Give the extent of all Babesia divergens-infected red blood cells.
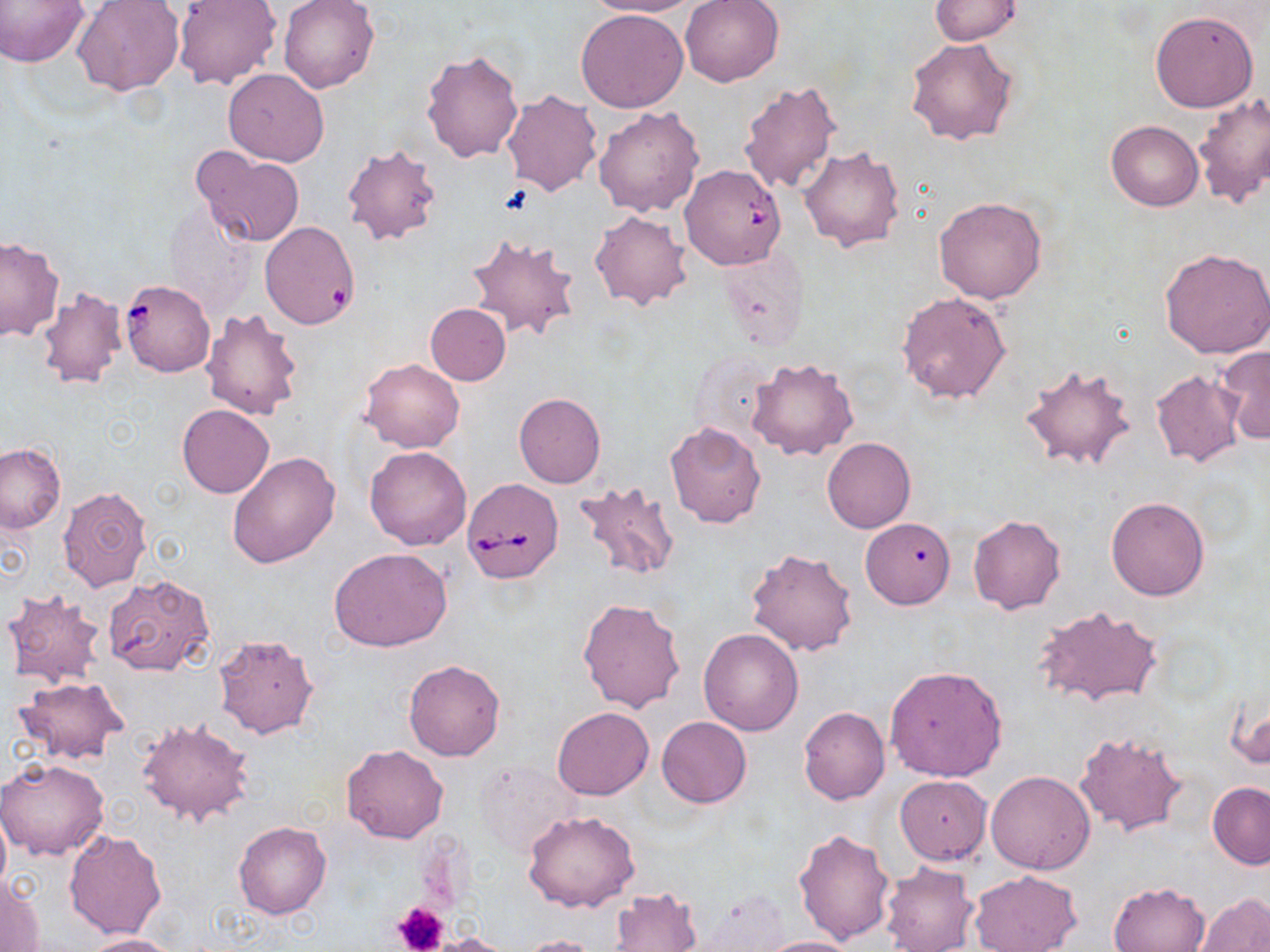

Approximate bounding boxes as (x1, y1, x2, y2) in pixels.
Babesia divergens-infected red blood cells: (678, 164, 786, 269), (119, 278, 216, 377), (461, 479, 565, 585).

Summary:
  - Uninfected red blood cell locations: (0, 0, 89, 67), (278, 0, 378, 94), (586, 0, 700, 17), (681, 0, 784, 86), (930, 0, 1021, 44), (74, 1, 184, 96), (175, 1, 281, 89), (575, 9, 688, 113), (1149, 10, 1259, 113), (906, 37, 1018, 146), (420, 48, 522, 162), (223, 68, 329, 166), (739, 80, 842, 195), (500, 88, 602, 196), (1192, 92, 1270, 209), (593, 105, 704, 217), (1106, 119, 1203, 211), (341, 144, 443, 245), (191, 146, 305, 247), (800, 147, 905, 253), (934, 197, 1048, 303), (162, 199, 255, 317), (589, 208, 693, 312), (260, 221, 361, 329), (466, 233, 581, 342), (0, 236, 65, 341), (718, 248, 811, 352), (1160, 248, 1270, 360), (37, 287, 129, 391), (897, 291, 1011, 404), (424, 303, 511, 385), (201, 309, 304, 419), (1216, 346, 1270, 444), (688, 347, 782, 445), (747, 357, 859, 461), (361, 359, 464, 453), (1019, 362, 1137, 473), (1150, 369, 1248, 469), (513, 393, 605, 488), (177, 404, 273, 498), (665, 422, 766, 528), (822, 437, 915, 533), (0, 443, 65, 532), (364, 445, 472, 551), (226, 451, 340, 569), (574, 477, 681, 582), (56, 486, 153, 593), (1105, 496, 1211, 601), (968, 516, 1066, 615), (861, 518, 955, 609), (746, 546, 858, 655), (329, 547, 452, 651), (104, 574, 215, 678), (2, 589, 106, 687), (577, 596, 686, 715), (1031, 606, 1163, 709), (699, 628, 803, 736), (213, 633, 320, 739), (404, 660, 505, 760), (885, 665, 1008, 781), (13, 676, 127, 765), (1226, 687, 1269, 771), (798, 707, 890, 806), (552, 708, 653, 800), (136, 717, 256, 827), (656, 717, 751, 807), (1074, 729, 1188, 838), (342, 745, 448, 843), (1, 758, 109, 860), (476, 758, 583, 857), (986, 770, 1095, 873), (894, 776, 992, 864), (1207, 783, 1270, 869), (0, 808, 10, 899), (524, 810, 639, 912), (234, 821, 331, 919), (792, 827, 896, 945), (64, 829, 167, 939), (880, 862, 979, 951), (970, 870, 1081, 952), (0, 875, 45, 951), (1109, 881, 1211, 952), (609, 888, 702, 951), (1195, 893, 1270, 952), (427, 932, 515, 952), (83, 934, 180, 952), (517, 935, 601, 952), (755, 936, 858, 952)
  - Platelet locations: (392, 898, 449, 952)
  - Slide-level diagnosis: Babesia divergens
  - Stain: May-Grünwald-Giemsa
  - Preparation: thin blood film
  - Field of view: single
  - Modality: optical microscopy
  - Image size: 1270×952 pixels
  - Magnification: 1000x